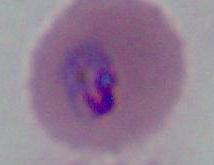

modality = micrograph
magnification = 400x or 1000x
identification = Plasmodium